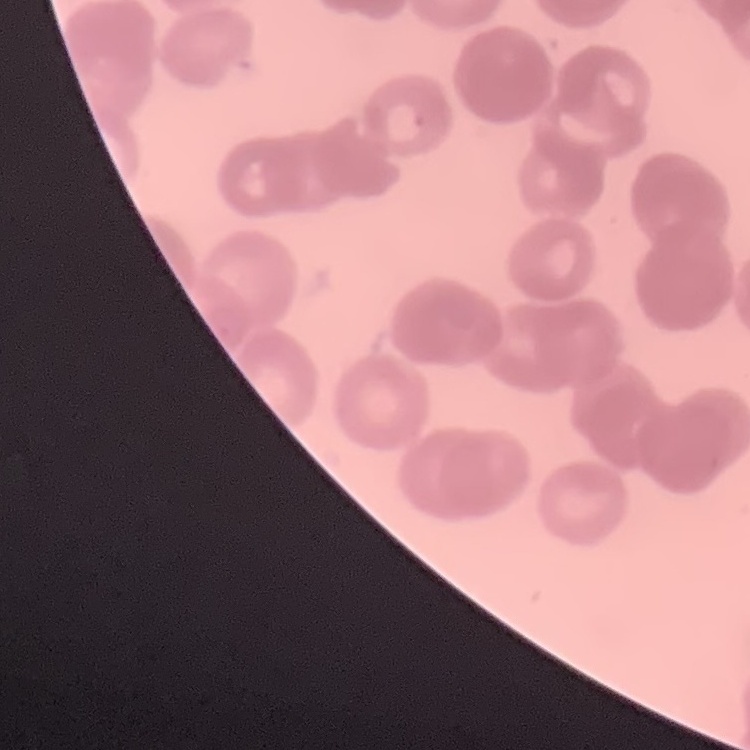

The erythrocytes exhibit rouleaux formation. Thin blood smear. Stained with either Field's or Giemsa. One tile cut from a larger photomicrograph.